Identify the cell.
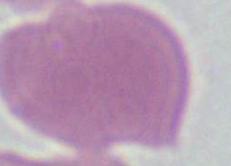

An erythrocyte.

modality = photomicrograph
magnification = 1000x